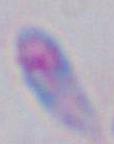

Toxoplasma gondii is shown. Photomicrograph. Captured at 1000x magnification.